Locate and identify every blood parasite.
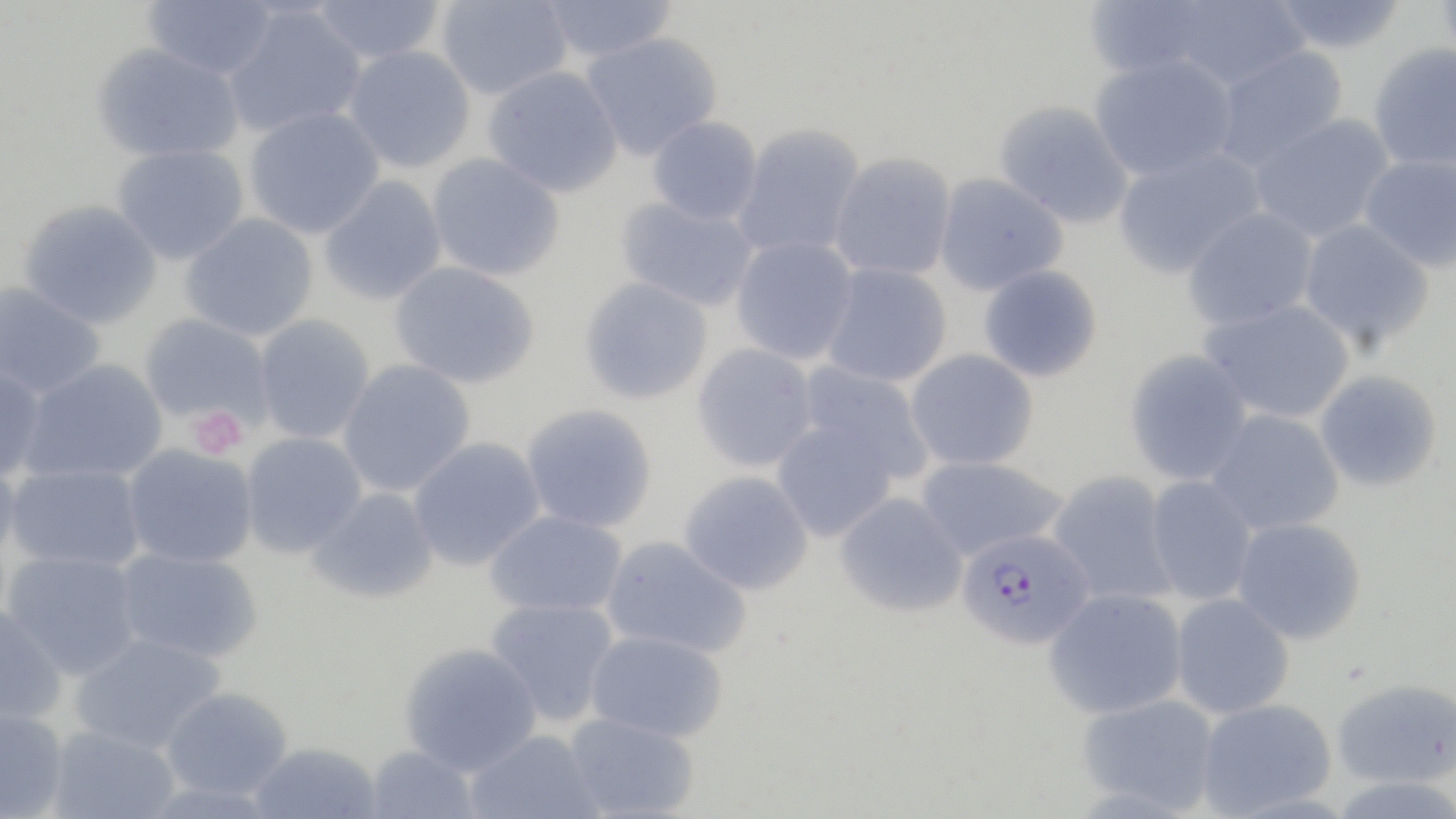
Approximate bounding boxes as [x1, y1, x2, y2] in pixels.
Plasmodium falciparum-infected red blood cells: [957, 528, 1094, 649].
No Plasmodium ovale, Plasmodium malariae, Plasmodium vivax, Babesia divergens, or Trypanosoma brucei observed.

slide-level diagnosis = Plasmodium falciparum
stain = May-Grünwald-Giemsa
uninfected red blood cell locations = approximate bounding boxes as [x1, y1, x2, y2] in pixels: [141, 0, 278, 81], [311, 0, 447, 65], [436, 0, 572, 100], [538, 0, 678, 63], [1083, 0, 1224, 80], [1160, 0, 1311, 90], [1269, 0, 1410, 54], [1434, 0, 1456, 70], [222, 6, 367, 138], [579, 31, 723, 162], [91, 42, 245, 164], [1367, 43, 1456, 172], [343, 45, 476, 173], [1210, 45, 1349, 171], [1089, 53, 1239, 181], [483, 66, 623, 198], [993, 100, 1134, 229], [244, 106, 384, 239], [1249, 113, 1396, 243], [647, 116, 763, 225], [731, 123, 867, 261], [111, 144, 249, 265], [1112, 147, 1266, 279], [829, 151, 957, 281], [426, 153, 565, 281], [1359, 153, 1456, 273], [933, 173, 1069, 296], [318, 175, 447, 306], [615, 195, 760, 312], [17, 199, 162, 330], [1182, 206, 1320, 331], [180, 213, 318, 341], [1297, 218, 1436, 351], [730, 235, 859, 365], [389, 262, 540, 389], [819, 262, 952, 388], [978, 264, 1103, 383], [578, 277, 714, 406], [0, 281, 106, 398], [1200, 297, 1356, 424], [138, 313, 274, 429], [253, 314, 375, 444], [691, 343, 819, 472], [904, 349, 1040, 471], [1124, 349, 1254, 486], [18, 359, 168, 484], [338, 359, 476, 497], [796, 362, 935, 485], [0, 364, 46, 482], [1314, 369, 1443, 493], [520, 404, 657, 533], [1206, 408, 1345, 536], [771, 419, 899, 542], [239, 431, 367, 558], [407, 437, 546, 571], [122, 444, 258, 569], [0, 451, 22, 567], [915, 455, 1067, 561], [6, 463, 146, 572], [679, 470, 814, 596], [1047, 470, 1177, 606], [1145, 476, 1257, 606], [306, 487, 439, 604], [834, 492, 968, 617], [485, 510, 627, 618], [1231, 516, 1366, 644], [600, 534, 752, 658], [115, 547, 263, 664], [3, 549, 142, 680], [1043, 587, 1188, 719], [1170, 592, 1295, 720], [485, 597, 620, 725], [0, 604, 67, 726], [585, 629, 729, 743], [69, 632, 226, 754], [398, 642, 542, 776], [1332, 677, 1456, 788], [160, 686, 294, 801], [1077, 693, 1220, 814], [1196, 697, 1338, 818], [0, 708, 70, 819], [563, 712, 699, 818], [47, 724, 181, 819], [465, 728, 603, 819], [248, 742, 383, 819], [363, 745, 482, 819]
field of view = single
image size = 1456×819 pixels
magnification = 1000x
preparation = thin blood film
modality = light microscopy
platelet locations = approximate bounding boxes as [x1, y1, x2, y2] in pixels: [186, 407, 248, 459]